Classify this cell by malaria status.
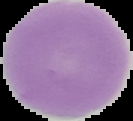

It is uninfected.

Summary:
  - Image type: segmented cell region with the area outside set to black
  - Preparation: thin blood smear
  - Image size: 133×121 pixels